Report the malaria status of this cell.
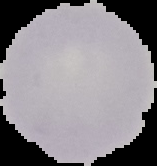
It is uninfected.

The area outside the segmented cell region is set to black. Image is 157×166 pixels. From a thin blood smear.